Identify the parasite.
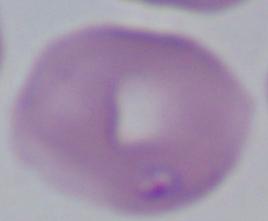
Babesia.

{
  "modality": "micrograph",
  "magnification": "1000x"
}